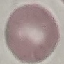

result = no malaria parasites seen
capture = smartphone through the microscope eyepiece
preparation = thin blood film
image type = cell patch, automatically extracted from a larger field of view and resized to 64 × 64 pixels
stain = Giemsa